Outline each blood parasite and name the species.
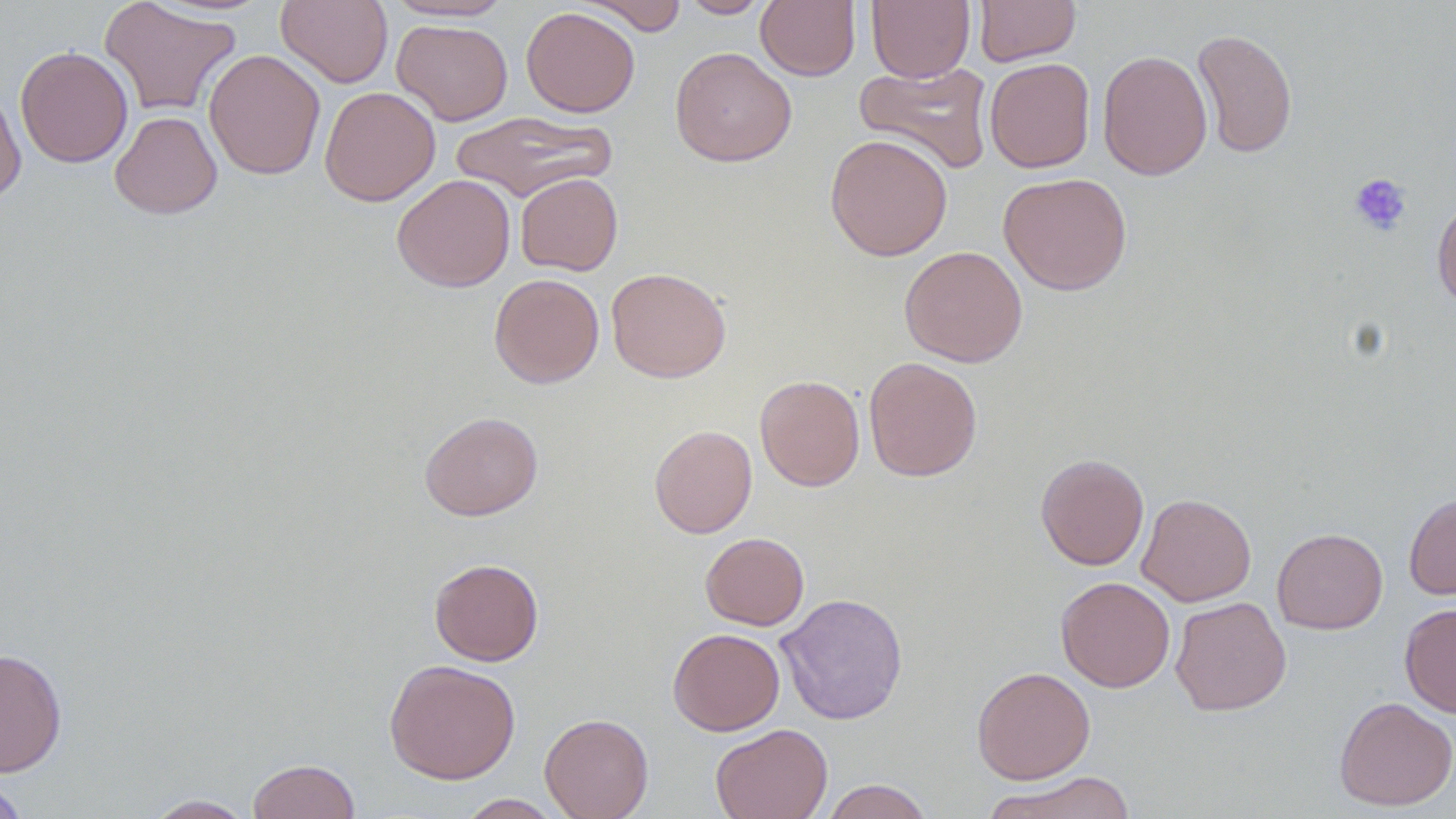

No blood parasites observed.

slide-level diagnosis = no evidence of blood parasites
modality = light microscopy
magnification = 1000x
preparation = thin blood film
uninfected red blood cell locations = approximate bounding boxes as [x1, y1, x2, y2] in pixels: [98, 0, 242, 117], [276, 0, 393, 88], [579, 0, 688, 36], [680, 0, 772, 18], [756, 0, 860, 81], [866, 0, 975, 82], [973, 0, 1081, 66], [385, 1, 515, 22], [521, 6, 640, 117], [391, 19, 513, 125], [1192, 28, 1298, 158], [14, 45, 133, 168], [670, 46, 797, 167], [204, 48, 325, 180], [1097, 49, 1212, 180], [984, 57, 1096, 173], [854, 60, 994, 175], [0, 83, 26, 205], [319, 86, 441, 206], [451, 110, 616, 204], [110, 111, 222, 219], [824, 134, 953, 261], [515, 172, 623, 275], [997, 172, 1133, 296], [392, 174, 515, 292], [1432, 194, 1456, 311], [899, 245, 1028, 367], [606, 267, 731, 383], [489, 273, 604, 388], [863, 357, 983, 482], [754, 374, 865, 491], [419, 411, 543, 520], [649, 424, 757, 538], [1035, 453, 1149, 570], [1404, 492, 1456, 599], [1136, 493, 1256, 607], [1272, 527, 1388, 634], [700, 531, 809, 631], [428, 558, 544, 665], [1055, 576, 1175, 692], [775, 592, 908, 725], [1170, 596, 1292, 716], [1399, 602, 1456, 718], [668, 627, 785, 735], [0, 648, 67, 777], [384, 659, 521, 784], [972, 666, 1095, 784], [1334, 696, 1456, 811], [539, 713, 654, 819], [710, 723, 833, 819], [247, 758, 360, 819], [981, 771, 1138, 819], [0, 778, 30, 819], [821, 779, 934, 819], [144, 794, 256, 818], [456, 794, 565, 818]
field of view = one of a larger specimen
platelet locations = approximate bounding boxes as [x1, y1, x2, y2] in pixels: [1348, 172, 1412, 236]
image size = 1456×819 pixels
stain = May-Grünwald-Giemsa